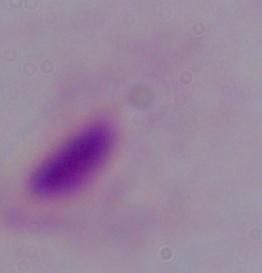
magnification: 1000x
identification: trichomonad
modality: micrograph